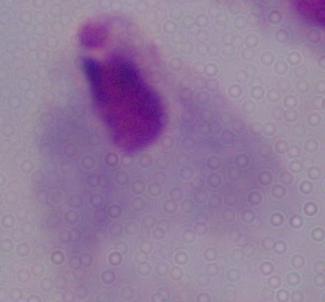
modality: micrograph
magnification: 1000x
identification: trichomonad